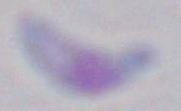
magnification = 1000x
identification = Toxoplasma gondii
modality = photomicrograph